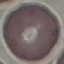

Summary:
  - Malaria status: uninfected
  - Stain: Giemsa
  - Preparation: thin smear
  - Image type: cell patch, automatically extracted from a larger field of view and resized to 64 × 64 pixels
  - Capture: smartphone camera at the microscope eyepiece